Assess this cell for malaria.
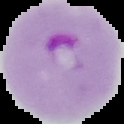
It is parasitized.

Image is 124×124 pixels. From a thin blood film. Segmented cell region on a black background.